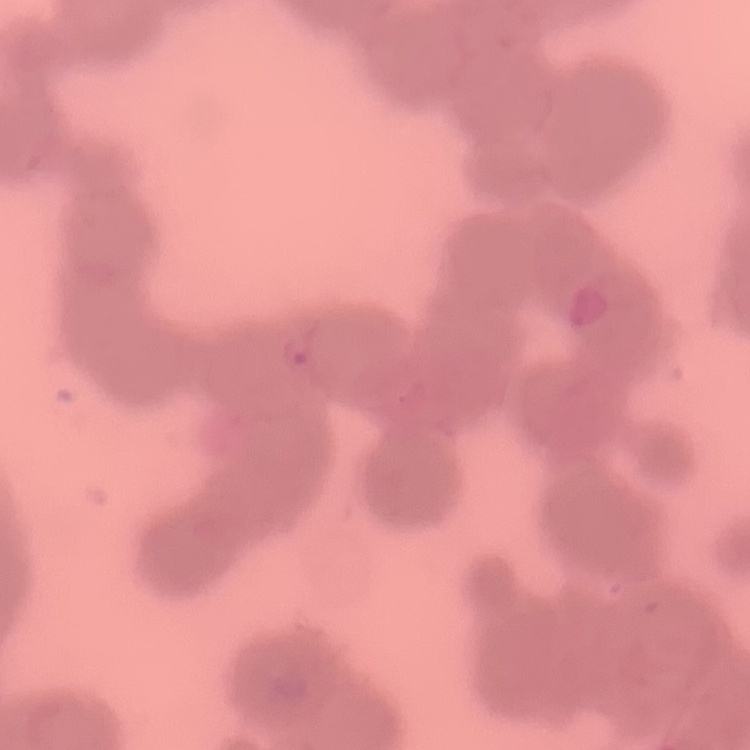 The erythrocytes exhibit rouleaux formation. Square crop of a larger photomicrograph. Stained with either Field's or Giemsa. Thin peripheral smear.